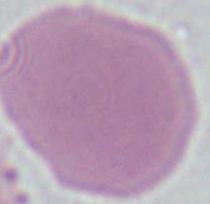

Summary:
  - Identification: erythrocyte
  - Magnification: 1000x
  - Modality: photomicrograph